Report the malaria status of this cell.
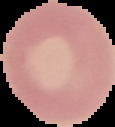

Uninfected.

Summary:
  - Image type: segmented cell region on a black background
  - Preparation: thin blood film
  - Image size: 115×127 pixels